Comment on the background quality.
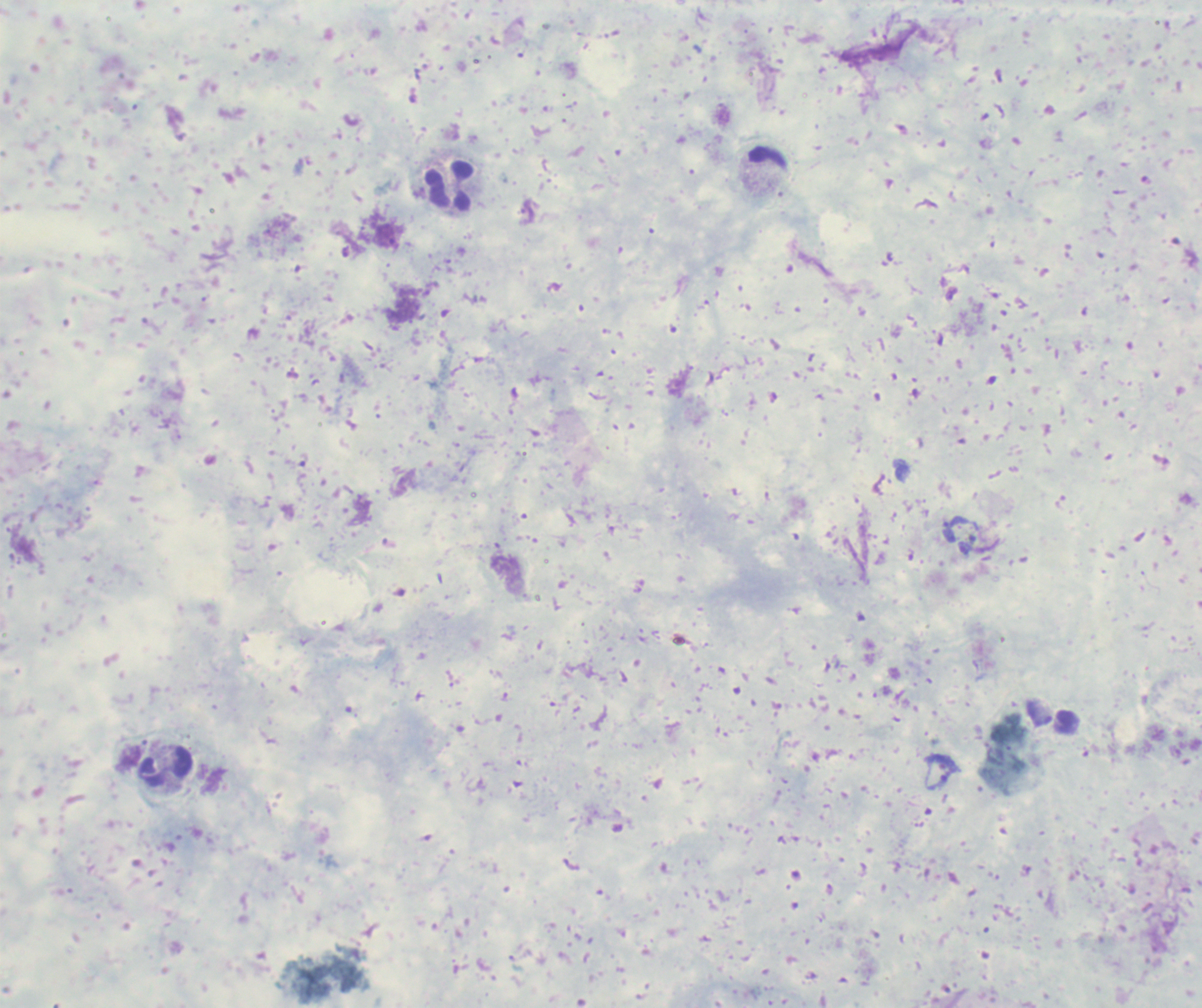

Unsatisfactory.

Approximate centers as (x, y) in pixels.
Summary:
  - Trophozoite locations: (942, 772)
  - Leukocyte locations: (449, 186), (166, 767)
  - Magnification: 100x
  - Result: Plasmodium parasites identified
  - Stain: Romanowsky
  - Context: previously used in an actual diagnosis
  - Field of view: single
  - Image size: 1202×1008 pixels
  - Preparation: thick blood film